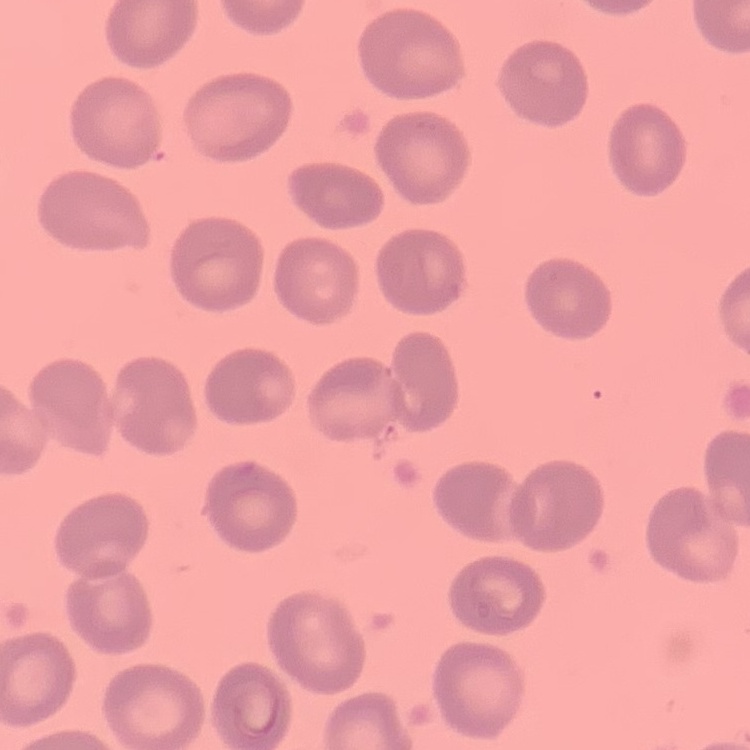

erythrocyte morphology = no rouleaux formation
image type = square crop of a larger photomicrograph
preparation = thin blood smear
stain = Field's or Giemsa